Comment on the morphology of the red blood cells.
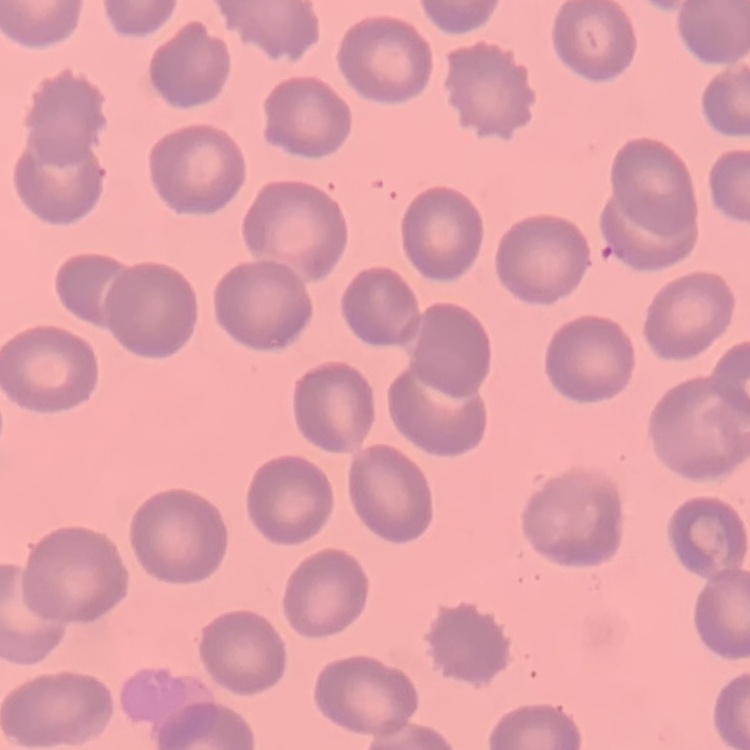

They show no rouleaux formation.

Field's or Giemsa stain. One tile cut from a larger photomicrograph. Thin blood smear.